Report the malaria status of this cell.
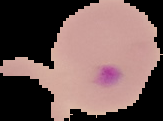
It is parasitized.

Summary:
  - Image size: 163×121 pixels
  - Preparation: thin blood smear
  - Image type: cell region segmented out of the field of view; surrounding area masked to black